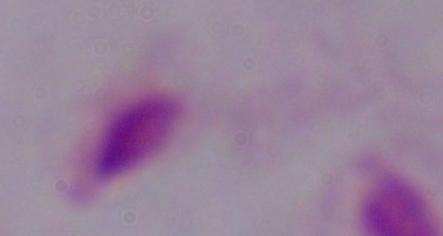

magnification = 1000x
identification = trichomonad
modality = photomicrograph